Identify the parasite.
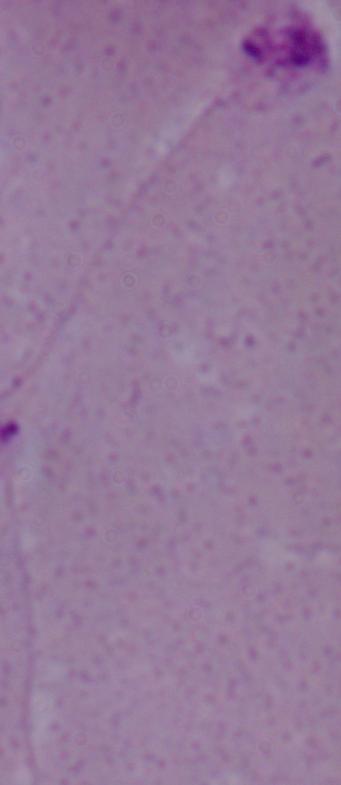

This is Leishmania.

{
  "magnification": "1000x",
  "modality": "photomicrograph"
}